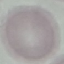

malaria_status: uninfected
image_type: automatically extracted cell patch, resized to 64 × 64 pixels
capture: smartphone camera at the microscope eyepiece
preparation: thin smear
stain: Giemsa